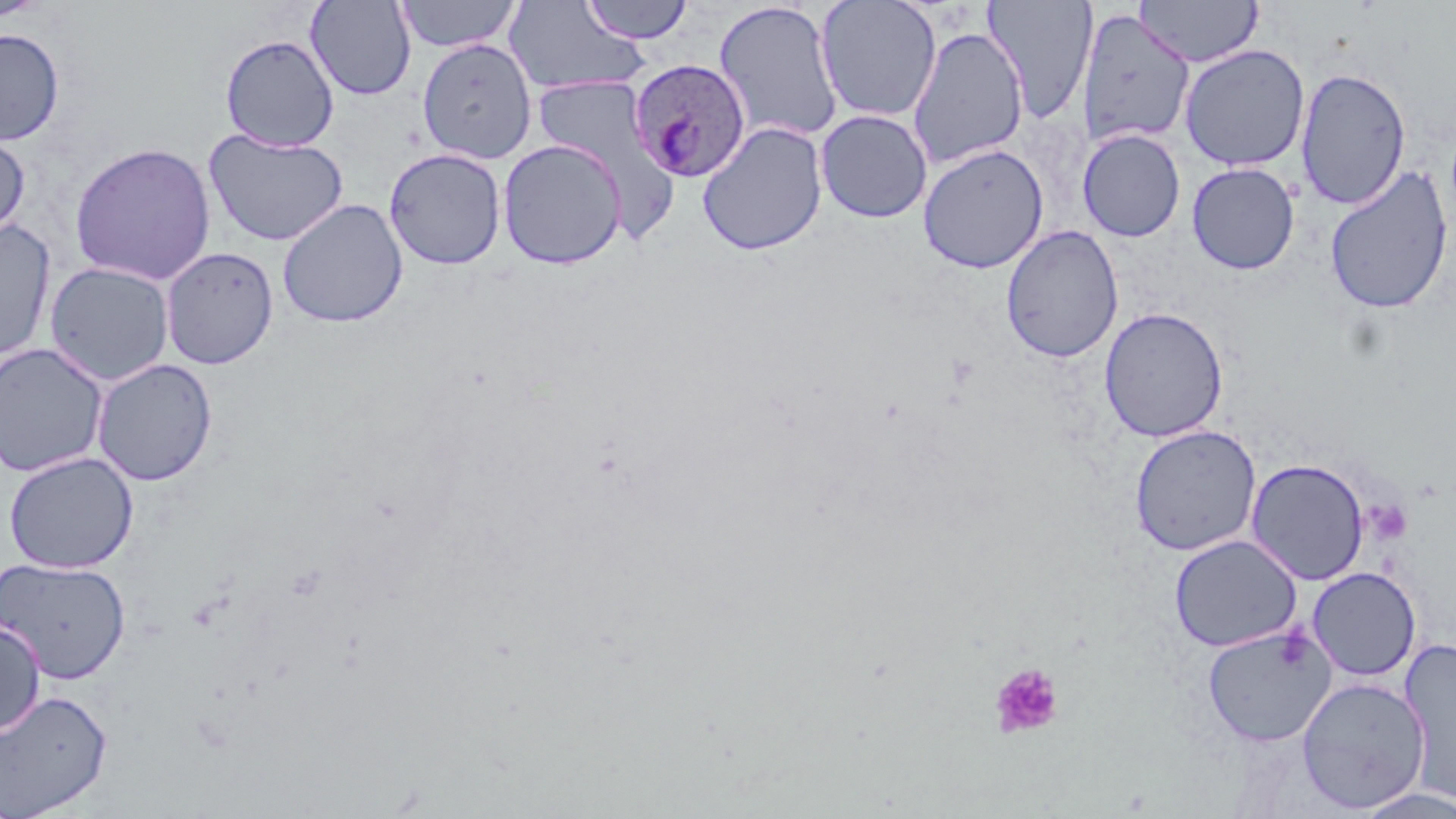
Summary:
  - Coordinate format: approximate bounding boxes as named x1/y1/x2/y2 corners in pixels
  - Plasmodium ovale-infected red blood cell locations: (x1=628, y1=60, x2=750, y2=181)
  - Platelet locations: (x1=1364, y1=498, x2=1413, y2=546), (x1=989, y1=663, x2=1064, y2=739)
  - Uninfected red blood cell locations: (x1=0, y1=0, x2=50, y2=21), (x1=305, y1=0, x2=417, y2=101), (x1=395, y1=0, x2=522, y2=53), (x1=579, y1=0, x2=694, y2=44), (x1=982, y1=0, x2=1098, y2=123), (x1=1134, y1=0, x2=1263, y2=67), (x1=713, y1=1, x2=844, y2=145), (x1=815, y1=1, x2=943, y2=122), (x1=502, y1=2, x2=650, y2=95), (x1=1077, y1=8, x2=1195, y2=149), (x1=907, y1=26, x2=1028, y2=169), (x1=0, y1=28, x2=65, y2=146), (x1=220, y1=34, x2=339, y2=151), (x1=416, y1=38, x2=538, y2=164), (x1=1179, y1=44, x2=1310, y2=172), (x1=1295, y1=66, x2=1411, y2=210), (x1=532, y1=76, x2=664, y2=191), (x1=815, y1=109, x2=932, y2=223), (x1=697, y1=122, x2=828, y2=256), (x1=0, y1=128, x2=30, y2=243), (x1=204, y1=129, x2=348, y2=246), (x1=1078, y1=129, x2=1185, y2=242), (x1=498, y1=140, x2=627, y2=270), (x1=69, y1=142, x2=216, y2=286), (x1=917, y1=143, x2=1049, y2=274), (x1=384, y1=148, x2=506, y2=270), (x1=1186, y1=162, x2=1300, y2=274), (x1=1324, y1=164, x2=1454, y2=315), (x1=277, y1=199, x2=408, y2=328), (x1=0, y1=221, x2=57, y2=366), (x1=1000, y1=225, x2=1123, y2=363), (x1=160, y1=247, x2=278, y2=369), (x1=44, y1=261, x2=175, y2=387), (x1=1099, y1=306, x2=1229, y2=442), (x1=0, y1=342, x2=108, y2=478), (x1=91, y1=358, x2=218, y2=486), (x1=1129, y1=425, x2=1261, y2=556), (x1=3, y1=452, x2=139, y2=574), (x1=1246, y1=458, x2=1370, y2=585), (x1=1169, y1=534, x2=1302, y2=652), (x1=0, y1=557, x2=131, y2=683), (x1=1306, y1=566, x2=1421, y2=681), (x1=0, y1=620, x2=46, y2=737), (x1=1201, y1=624, x2=1336, y2=746), (x1=1397, y1=638, x2=1456, y2=806), (x1=1296, y1=677, x2=1430, y2=812), (x1=0, y1=689, x2=113, y2=818), (x1=1352, y1=786, x2=1456, y2=818)
  - Slide-level diagnosis: Plasmodium ovale
  - Magnification: 1000x
  - Image size: 1456×819 pixels
  - Stain: May-Grünwald-Giemsa
  - Field of view: single
  - Modality: light microscopy
  - Preparation: thin blood smear